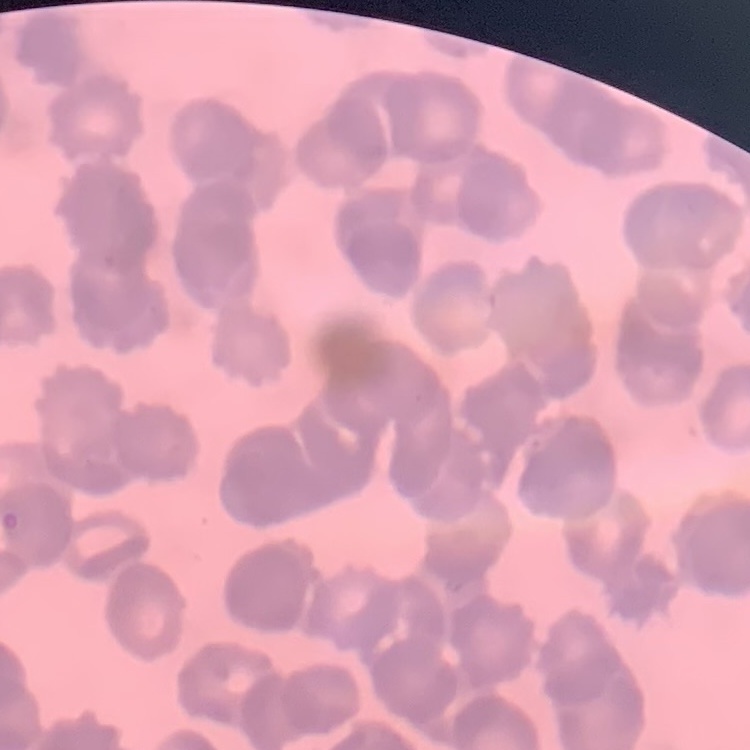

Summary:
  - Erythrocyte morphology: rouleaux formation
  - Preparation: thin blood smear
  - Stain: Field's or Giemsa
  - Image type: square crop of a larger photomicrograph